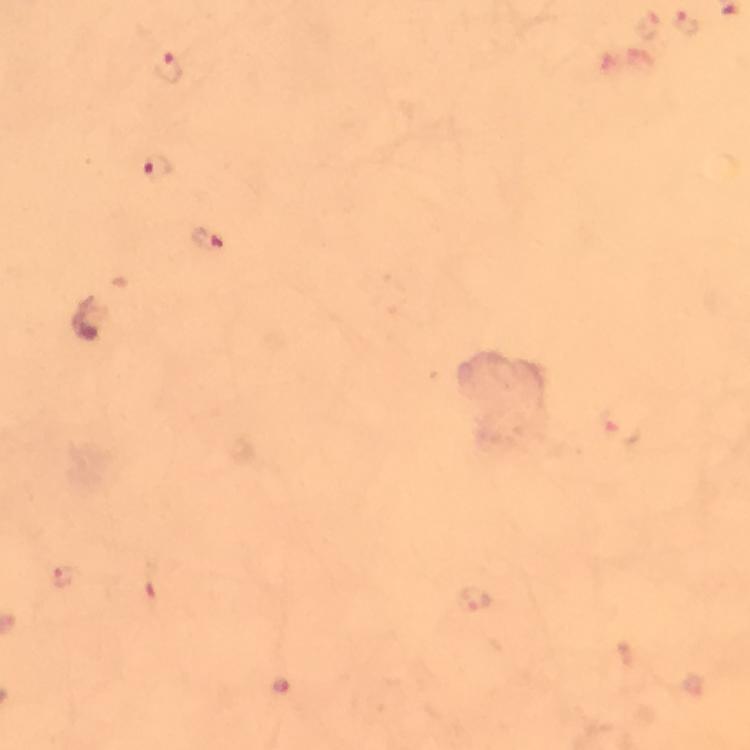 Approximate object centers, in pixels from the top-left corner. Plasmodium parasite locations: (x=687, y=23), (x=648, y=26), (x=166, y=68), (x=159, y=168), (x=209, y=240), (x=617, y=429), (x=64, y=576), (x=476, y=599), (x=280, y=685). 100x magnification. Thick blood smear. Image is 750×750 pixels. A crop from one field of view. Giemsa stain. Photographed through the microscope with a smartphone camera. Immersion oil applied. From a diagnostic examination for malaria.